Outline each blood parasite and name the species.
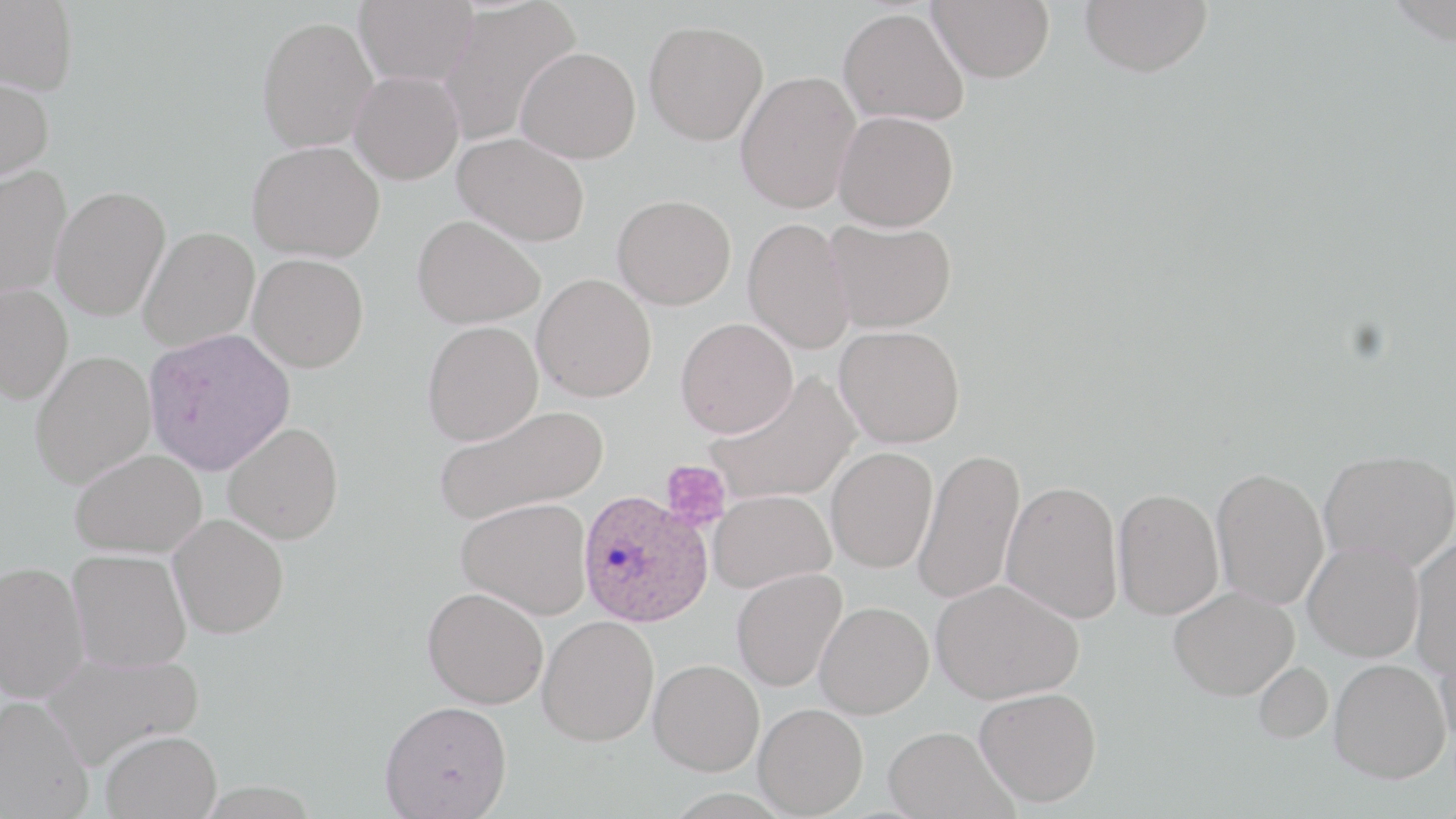

Approximate bounding boxes as [x1, y1, x2, y2] in pixels.
Plasmodium ovale-infected red blood cells: [577, 490, 712, 627].
No Plasmodium falciparum, Plasmodium malariae, Plasmodium vivax, Babesia divergens, or Trypanosoma brucei observed.

slide-level diagnosis = Plasmodium ovale
platelet locations = approximate bounding boxes as [x1, y1, x2, y2] in pixels: [660, 460, 732, 533]
preparation = thin blood film
magnification = 1000x
image size = 1456×819 pixels
stain = May-Grünwald-Giemsa
uninfected red blood cell locations = approximate bounding boxes as [x1, y1, x2, y2] in pixels: [0, 0, 79, 94], [354, 0, 479, 85], [436, 0, 580, 147], [928, 0, 1054, 83], [1079, 0, 1213, 77], [838, 7, 969, 127], [257, 15, 378, 153], [644, 20, 768, 145], [516, 46, 641, 164], [349, 70, 464, 184], [735, 71, 860, 213], [0, 75, 54, 183], [833, 110, 959, 231], [454, 132, 592, 246], [248, 140, 385, 263], [0, 165, 72, 299], [49, 185, 170, 320], [612, 194, 736, 309], [412, 213, 546, 329], [742, 218, 854, 354], [824, 218, 957, 333], [138, 226, 259, 351], [248, 253, 369, 372], [532, 273, 657, 402], [0, 283, 73, 404], [675, 317, 798, 438], [422, 321, 543, 446], [834, 325, 965, 447], [149, 330, 296, 476], [30, 350, 156, 488], [704, 370, 859, 505], [435, 405, 608, 526], [223, 422, 343, 544], [826, 446, 938, 573], [70, 448, 207, 558], [913, 448, 1025, 605], [1319, 449, 1456, 571], [1211, 466, 1329, 610], [1001, 480, 1124, 625], [1112, 487, 1224, 620], [709, 490, 835, 593], [456, 497, 592, 619], [168, 514, 289, 638], [1408, 535, 1456, 678], [1303, 541, 1424, 662], [67, 549, 191, 673], [0, 560, 89, 703], [731, 568, 847, 691], [929, 578, 1083, 704], [1169, 585, 1299, 700], [422, 587, 548, 708], [815, 600, 933, 718], [537, 615, 659, 746], [1435, 629, 1456, 754], [42, 651, 205, 768], [649, 658, 764, 775], [1329, 659, 1450, 782], [1254, 661, 1332, 743], [974, 687, 1102, 807], [0, 694, 94, 819], [380, 700, 513, 818], [754, 703, 868, 817], [883, 725, 1013, 819], [100, 729, 221, 818]
field of view = single
modality = light microscopy